Classify this cell by malaria status.
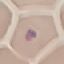

It is uninfected.

Giemsa stain. Photographed with a smartphone camera at the microscope eyepiece. Thin blood film. Automatically extracted cell patch, resized to 64 × 64 pixels.